Name the parasite shown.
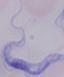
This is a trypanosome.

magnification: 1000x
modality: photomicrograph